Assess this cell for malaria.
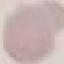

It is uninfected.

Thin blood film. Automatically extracted cell patch, resized to 64 × 64 pixels. Giemsa-stained preparation. Photographed with a smartphone camera at the microscope eyepiece.